Identify the parasite.
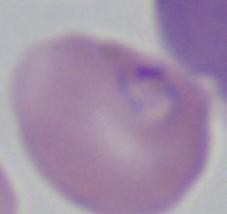

This is Babesia.

Micrograph. Captured at 1000x magnification.